Report the malaria status of this cell.
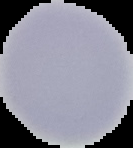

Uninfected.

{
  "image_type": "segmented cell region on a black background",
  "image_size": "133×148 pixels",
  "preparation": "thin blood smear"
}